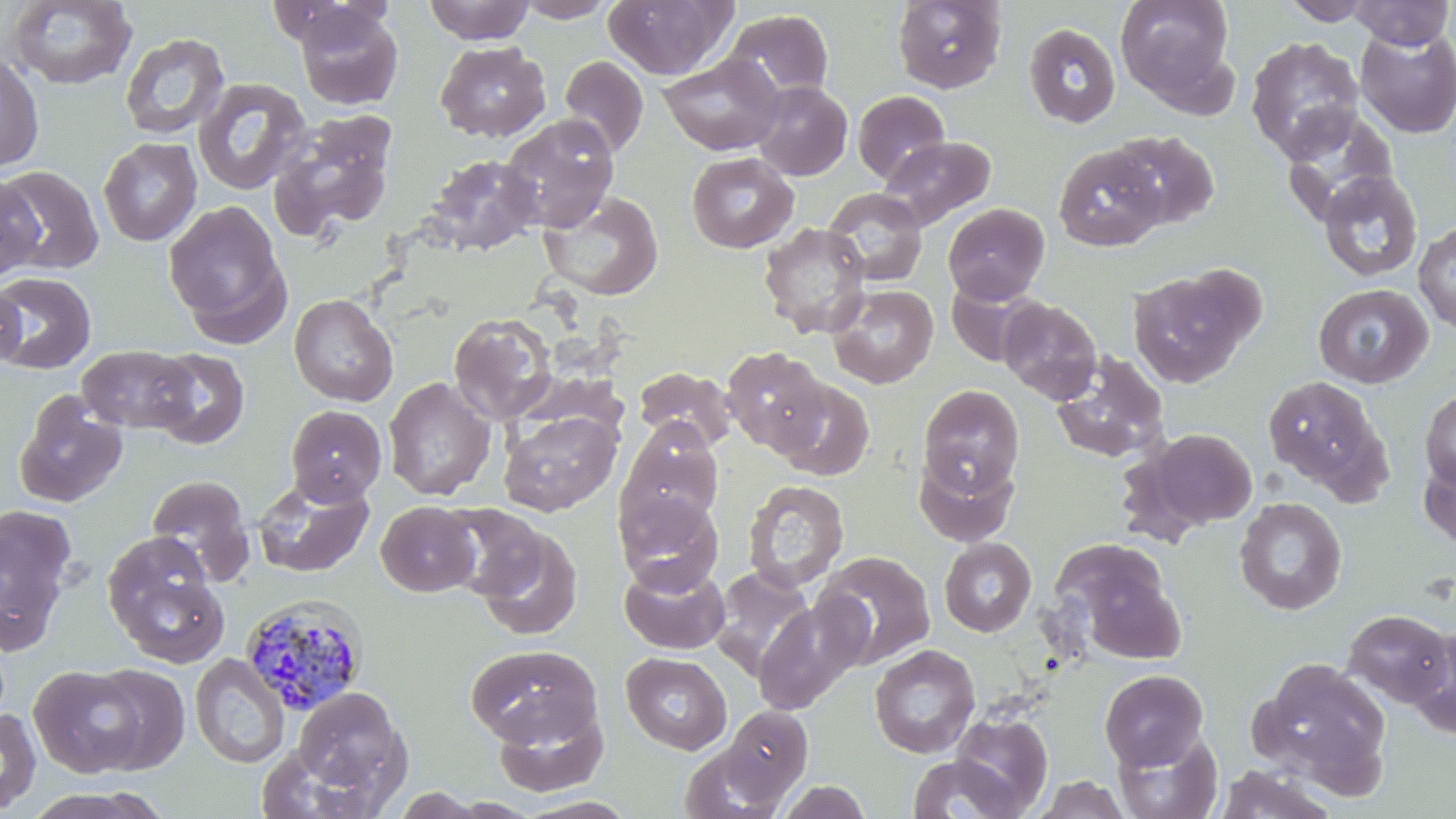
Approximate bounding boxes as (x1, y1, x2, y2) in pixels. Plasmodium malariae-infected red blood cell locations: (238, 594, 369, 716). Uninfected red blood cell locations: (4, 0, 139, 90), (423, 0, 535, 44), (513, 0, 619, 22), (892, 0, 1007, 93), (1114, 0, 1236, 106), (1281, 0, 1377, 25), (1346, 0, 1454, 49), (602, 1, 736, 80), (293, 4, 402, 111), (722, 9, 834, 102), (1023, 22, 1122, 128), (1354, 27, 1456, 139), (119, 32, 230, 140), (1245, 36, 1364, 162), (435, 41, 551, 142), (0, 50, 44, 172), (658, 54, 785, 155), (559, 55, 649, 159), (192, 78, 311, 195), (750, 81, 852, 180), (852, 90, 951, 186), (1278, 107, 1399, 225), (266, 111, 398, 242), (499, 113, 620, 232), (1108, 130, 1220, 229), (879, 135, 995, 230), (98, 136, 202, 246), (1053, 144, 1167, 251), (686, 152, 799, 254), (426, 153, 541, 255), (0, 165, 104, 275), (1317, 170, 1423, 283), (0, 173, 44, 281), (822, 188, 928, 286), (539, 190, 664, 300), (164, 201, 288, 335), (943, 203, 1050, 304), (758, 222, 871, 338), (1414, 223, 1456, 334), (1127, 266, 1261, 388), (0, 271, 96, 374), (945, 279, 1041, 366), (0, 281, 25, 372), (828, 284, 939, 388), (1313, 284, 1433, 388), (289, 293, 398, 406), (998, 297, 1102, 403), (449, 312, 558, 424), (77, 345, 198, 433), (721, 346, 831, 455), (146, 347, 250, 450), (1049, 352, 1170, 464), (634, 365, 738, 452), (1262, 373, 1388, 496), (383, 377, 496, 500), (773, 378, 875, 480), (917, 384, 1025, 498), (13, 390, 128, 508), (1420, 390, 1456, 489), (285, 405, 386, 505), (498, 409, 622, 516), (617, 422, 723, 533), (1146, 428, 1257, 530), (913, 451, 1019, 547), (1418, 451, 1456, 551), (145, 474, 255, 582), (252, 476, 375, 578), (743, 479, 849, 592), (614, 490, 724, 595), (1234, 497, 1347, 615), (376, 500, 480, 597), (437, 503, 549, 603), (0, 504, 78, 656), (472, 524, 584, 641), (102, 533, 229, 667), (939, 537, 1037, 637), (1056, 548, 1187, 663), (812, 551, 936, 669), (619, 560, 730, 655), (710, 566, 815, 678), (753, 599, 866, 713), (1342, 609, 1454, 707), (1406, 626, 1456, 739), (465, 644, 603, 749), (869, 644, 980, 759), (621, 652, 733, 754), (189, 653, 290, 769), (1253, 658, 1392, 789), (83, 663, 191, 774), (29, 665, 148, 777), (1099, 669, 1209, 769), (290, 685, 412, 809), (492, 700, 609, 798), (720, 704, 814, 808), (0, 707, 41, 815), (950, 711, 1053, 816), (1112, 727, 1223, 819), (681, 741, 792, 819), (906, 754, 1022, 819), (1213, 765, 1338, 819), (1030, 775, 1132, 818), (775, 780, 873, 819). Slide-level diagnosis: Plasmodium malariae. May-Grünwald-Giemsa stain. Thin blood film. Image is 1456×819 pixels. One field of a larger specimen. 1000x magnification. Light microscopy.